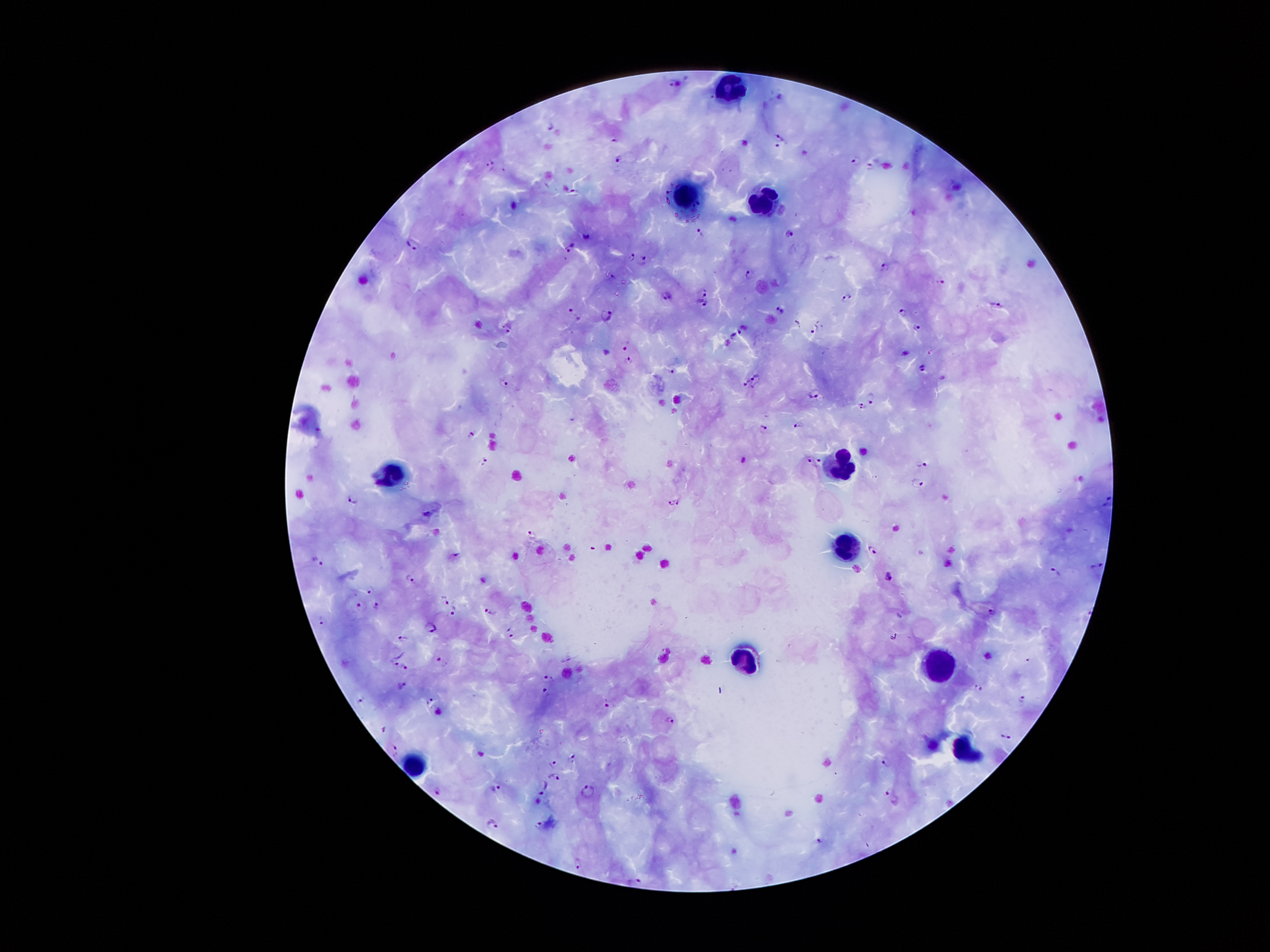

Approximate centers as [x, y] in pixels.
Summary:
  - Leukocyte locations: [727, 91], [684, 192], [766, 207], [842, 469], [390, 477], [849, 551], [945, 659], [744, 662], [961, 749], [413, 767]
  - Malaria parasite locations: [675, 83], [778, 97], [550, 126], [778, 135], [615, 139], [776, 146], [621, 158], [857, 161], [491, 164], [870, 165], [574, 191], [701, 232], [790, 233], [588, 236], [413, 245], [568, 249], [632, 257], [565, 259], [642, 261], [884, 266], [748, 274], [613, 277], [940, 281], [702, 292], [668, 296], [847, 297], [703, 303], [998, 303], [780, 308], [902, 311], [576, 314], [607, 314], [798, 323], [507, 327], [814, 327], [918, 328], [739, 331], [734, 335], [625, 345], [905, 352], [630, 360], [922, 369], [672, 371], [746, 381], [503, 383], [815, 394], [870, 396], [862, 406], [798, 424], [764, 427], [471, 434], [819, 459], [483, 461], [809, 461], [922, 465], [917, 483], [352, 500], [1108, 501], [679, 502], [671, 503], [427, 514], [532, 535], [873, 548], [457, 555], [322, 563], [1097, 566], [1055, 570], [888, 576], [411, 578], [370, 589], [446, 598], [362, 605], [377, 605], [453, 609], [491, 611], [991, 611], [322, 619], [432, 628], [513, 635], [402, 638], [1027, 659], [441, 660], [396, 662], [405, 665], [549, 678], [403, 684], [978, 688], [546, 691], [360, 698], [1021, 699], [431, 700], [607, 702], [669, 720], [382, 729], [1005, 736], [395, 748], [572, 756], [553, 762], [884, 762], [556, 777], [544, 786], [496, 788], [437, 790], [588, 790], [889, 792], [491, 823], [539, 824], [819, 841], [577, 862], [637, 880]
  - Image size: 1270×952 pixels
  - Patient malaria status: positive for Plasmodium falciparum
  - Field of view: one from this slide
  - Stain: Giemsa
  - Preparation: thick blood film
  - Magnification: 100x
  - Capture: smartphone camera through the microscope eyepiece